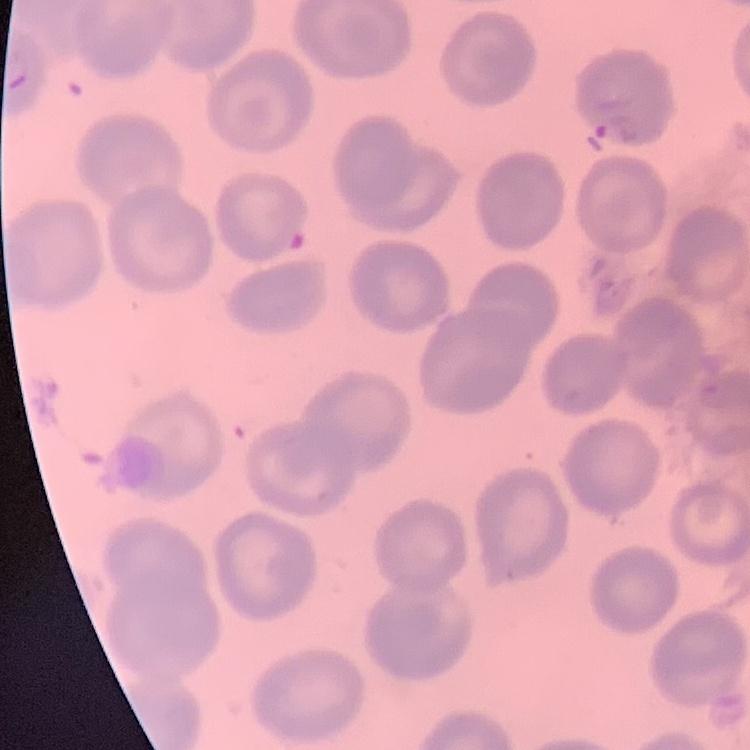 The red blood cells exhibit no rouleaux formation. Field's or Giemsa stain. Thin blood smear. Square crop of a larger photomicrograph.